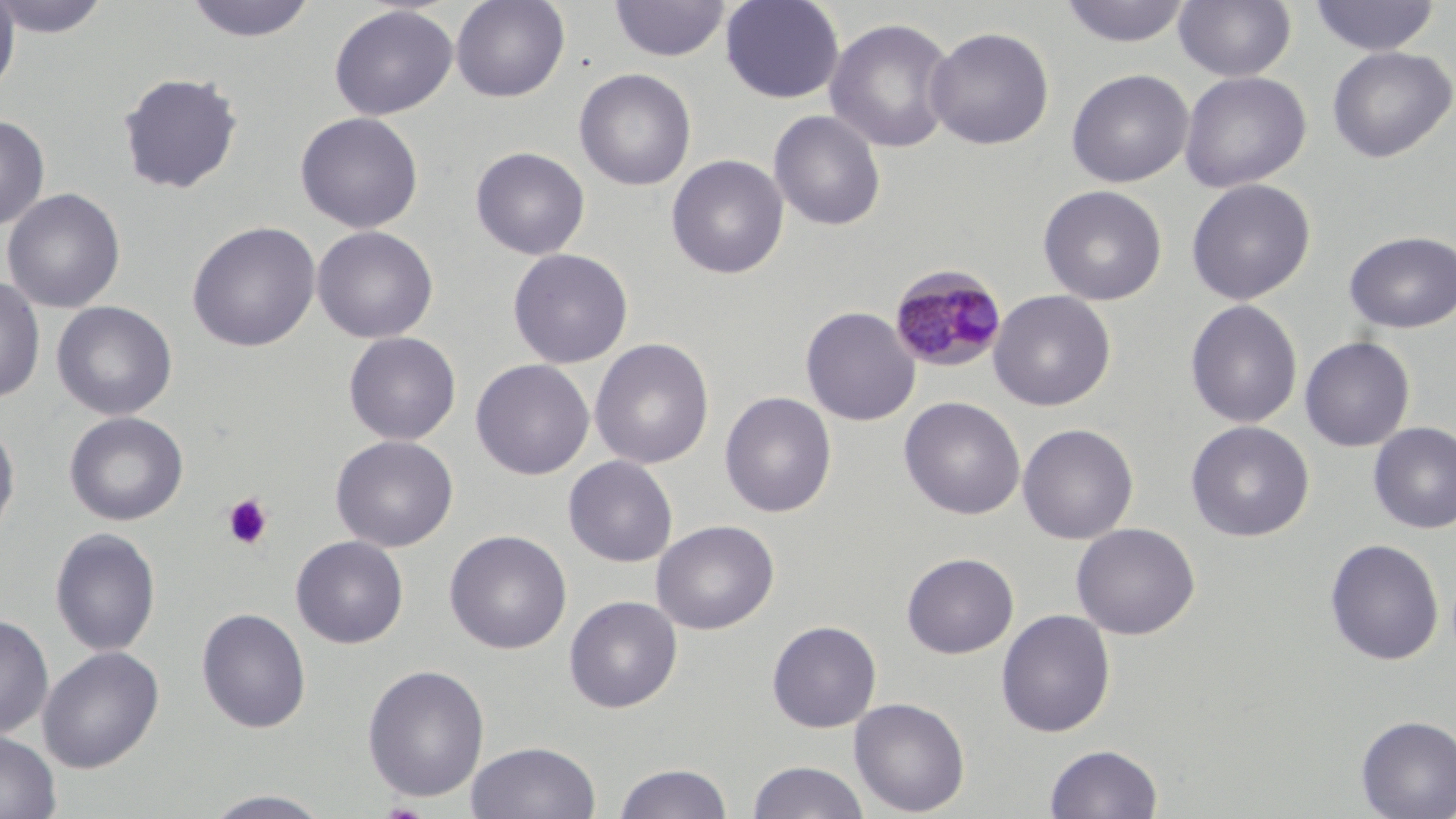

slide-level diagnosis = Plasmodium malariae
field of view = single
uninfected red blood cell locations = approximate bounding boxes as (x1, y1, x2, y2) in pixels: (0, 0, 113, 39), (182, 0, 319, 44), (450, 0, 570, 103), (610, 0, 730, 62), (720, 0, 845, 104), (1058, 0, 1192, 47), (1174, 0, 1296, 82), (1309, 0, 1440, 57), (0, 1, 20, 99), (329, 5, 458, 120), (824, 17, 958, 154), (925, 25, 1055, 151), (1326, 45, 1455, 163), (573, 68, 696, 191), (1066, 69, 1194, 188), (118, 71, 244, 194), (1179, 71, 1311, 193), (768, 109, 886, 232), (295, 112, 424, 233), (0, 114, 50, 231), (471, 146, 590, 260), (666, 154, 789, 279), (1186, 178, 1316, 305), (1038, 185, 1167, 306), (2, 188, 126, 314), (186, 221, 321, 352), (312, 225, 438, 343), (1344, 231, 1456, 333), (508, 248, 633, 368), (0, 276, 46, 405), (988, 289, 1116, 411), (1185, 299, 1303, 429), (51, 301, 178, 421), (800, 306, 921, 426), (343, 332, 461, 445), (1299, 336, 1415, 452), (589, 338, 714, 470), (470, 359, 595, 480), (719, 391, 837, 518), (899, 396, 1025, 520), (64, 411, 189, 526), (0, 419, 20, 545), (1186, 421, 1314, 542), (1368, 422, 1456, 534), (1017, 423, 1139, 545), (331, 435, 458, 552), (563, 455, 678, 567), (651, 519, 779, 635), (1071, 522, 1200, 639), (50, 527, 161, 657), (444, 530, 572, 654), (291, 535, 408, 649), (1324, 538, 1444, 666), (901, 552, 1019, 658), (564, 595, 682, 712), (196, 607, 311, 734), (996, 608, 1116, 737), (0, 614, 54, 739), (767, 620, 882, 733), (38, 646, 164, 773), (362, 663, 490, 803), (849, 697, 970, 816), (1355, 714, 1456, 818), (0, 730, 61, 819), (467, 741, 600, 819), (1044, 743, 1163, 818), (746, 760, 871, 819), (613, 762, 734, 819), (195, 788, 338, 818)
stain = May-Grünwald-Giemsa
preparation = thin blood smear
platelet locations = approximate bounding boxes as (x1, y1, x2, y2) in pixels: (221, 493, 274, 550)
Plasmodium malariae-infected red blood cell locations = approximate bounding boxes as (x1, y1, x2, y2) in pixels: (889, 265, 1008, 373)
image size = 1456×819 pixels
magnification = 1000x
modality = light microscopy